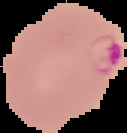

{
  "image_size": "127×133 pixels",
  "image_type": "segmented cell region on a black background",
  "preparation": "thin blood film",
  "malaria_status": "parasitized"
}